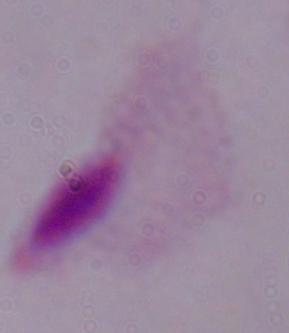
modality = photomicrograph
magnification = 1000x
identification = trichomonad